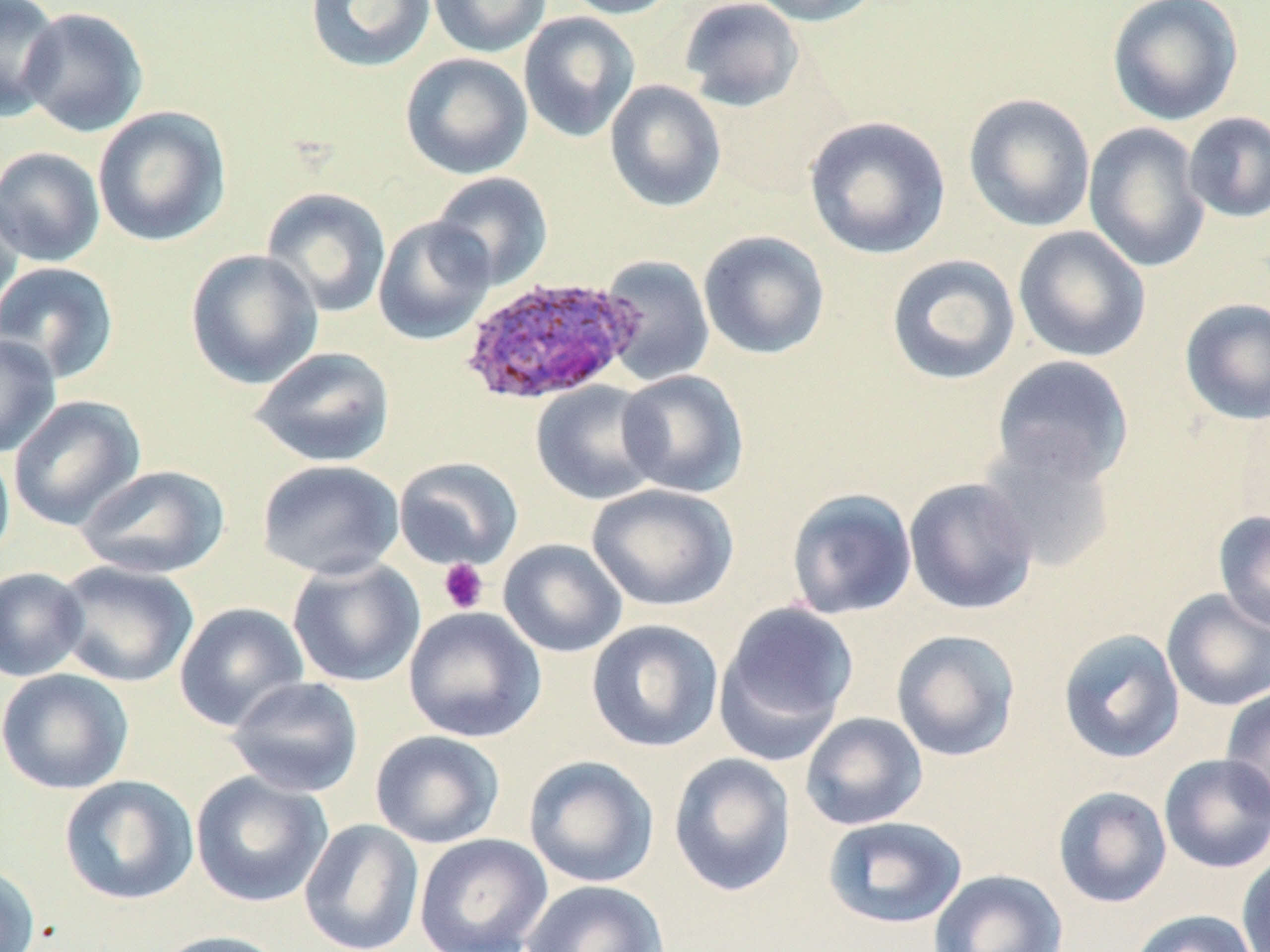
Summary:
  - Coordinate format: approximate bounding boxes as [x1, y1, x2, y2] in pixels
  - Platelet locations: [438, 558, 489, 614]
  - Plasmodium ovale-infected red blood cell locations: [459, 276, 641, 406]
  - Uninfected red blood cell locations: [0, 0, 63, 122], [304, 0, 436, 73], [427, 0, 552, 58], [559, 0, 685, 19], [679, 0, 805, 112], [748, 0, 883, 26], [1106, 0, 1244, 126], [17, 7, 149, 137], [518, 11, 640, 143], [399, 52, 533, 180], [605, 80, 726, 212], [962, 93, 1096, 233], [93, 106, 232, 248], [1183, 111, 1270, 224], [804, 115, 951, 260], [1082, 122, 1212, 273], [0, 146, 106, 267], [429, 171, 553, 290], [0, 186, 26, 325], [261, 187, 392, 318], [372, 216, 496, 346], [1013, 225, 1152, 363], [697, 230, 831, 360], [185, 249, 324, 389], [598, 254, 715, 385], [885, 254, 1021, 386], [0, 261, 120, 383], [1179, 297, 1270, 425], [0, 333, 61, 456], [250, 346, 396, 467], [991, 355, 1135, 487], [615, 368, 749, 498], [530, 381, 665, 506], [8, 395, 146, 532], [976, 437, 1119, 573], [0, 444, 15, 567], [393, 457, 524, 570], [257, 459, 405, 581], [75, 464, 230, 579], [903, 477, 1039, 615], [587, 483, 738, 611], [785, 487, 918, 620], [1213, 510, 1270, 634], [498, 538, 627, 657], [286, 556, 425, 688], [53, 560, 199, 688], [0, 566, 89, 681], [1161, 589, 1270, 712], [715, 601, 860, 759], [174, 602, 309, 731], [403, 606, 546, 743], [586, 619, 724, 753], [890, 628, 1021, 762], [1058, 628, 1185, 764], [0, 668, 134, 795], [226, 676, 364, 797], [1220, 686, 1270, 819], [799, 712, 928, 831], [369, 730, 505, 848], [668, 752, 797, 897], [1158, 753, 1270, 873], [523, 755, 659, 888], [189, 770, 333, 907], [59, 775, 199, 906], [1052, 785, 1172, 909], [822, 815, 967, 929], [298, 818, 424, 952], [413, 833, 552, 952], [1236, 853, 1270, 952], [0, 862, 41, 952], [929, 869, 1068, 952], [520, 879, 669, 952], [1128, 908, 1258, 952], [151, 930, 288, 952]
  - Slide-level diagnosis: Plasmodium ovale
  - Stain: May-Grünwald-Giemsa
  - Modality: light microscopy
  - Preparation: thin blood smear
  - Image size: 1270×952 pixels
  - Field of view: one of a larger specimen
  - Magnification: 1000x